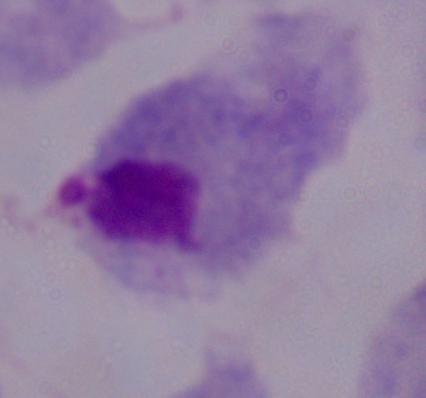

magnification: 1000x
modality: micrograph
identification: trichomonad